Assess this cell for malaria.
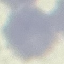
It is uninfected.

{
  "image_type": "cell patch, automatically extracted from a larger field of view and resized to 64 × 64 pixels",
  "capture": "smartphone through the microscope eyepiece",
  "stain": "Giemsa",
  "preparation": "thin blood film"
}